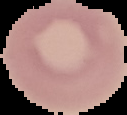
Summary:
  - Image size: 127×115 pixels
  - Image type: segmented cell region on a black background
  - Preparation: thin blood film
  - Malaria status: uninfected